Evaluate for malaria.
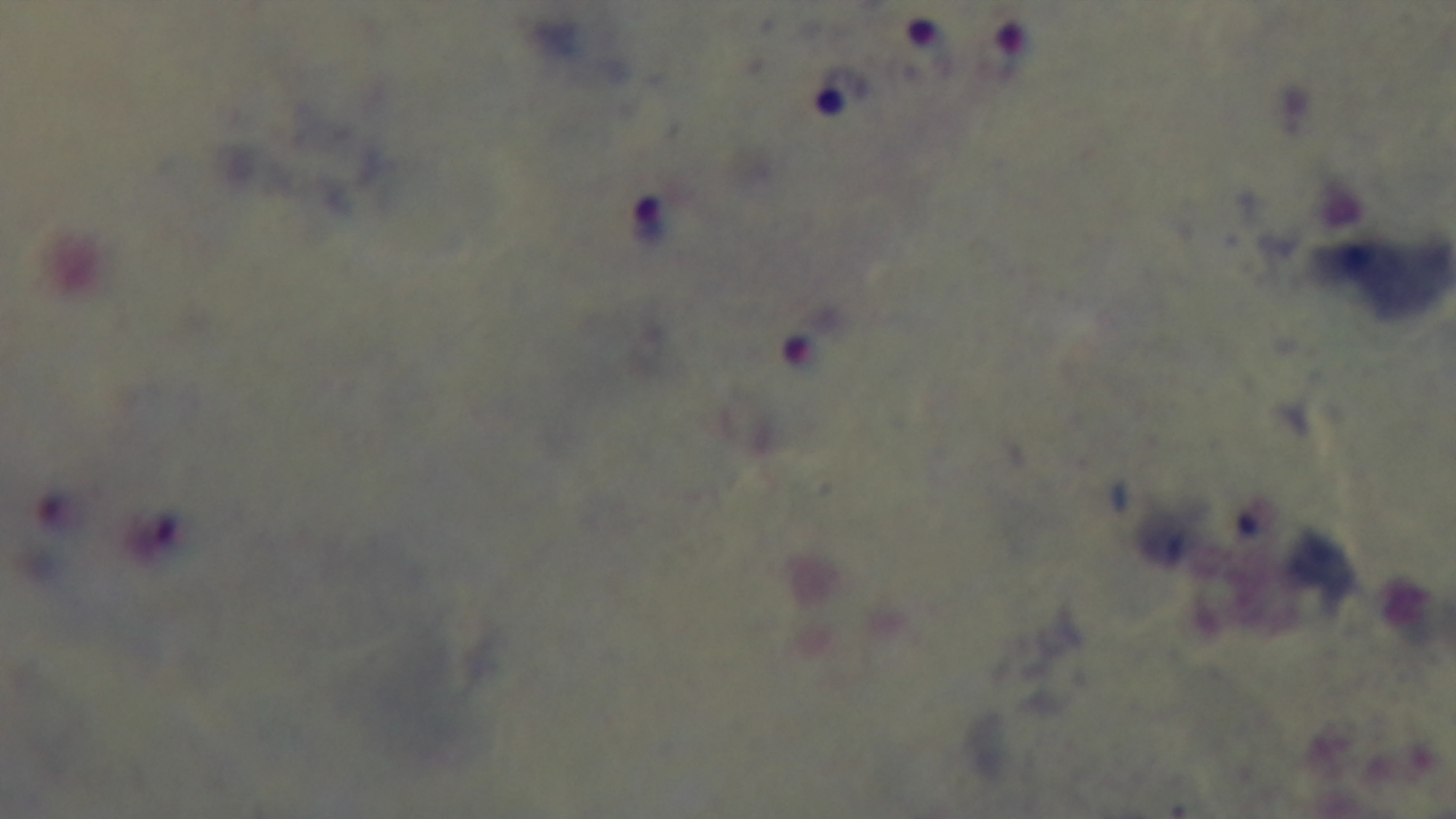

Positive.

{
  "field_of_view": "single",
  "preparation": "thick smear",
  "modality": "light microscopy",
  "stain": "Giemsa",
  "objective": "100x oil immersion",
  "capture": "mounted 4K digital camera"
}